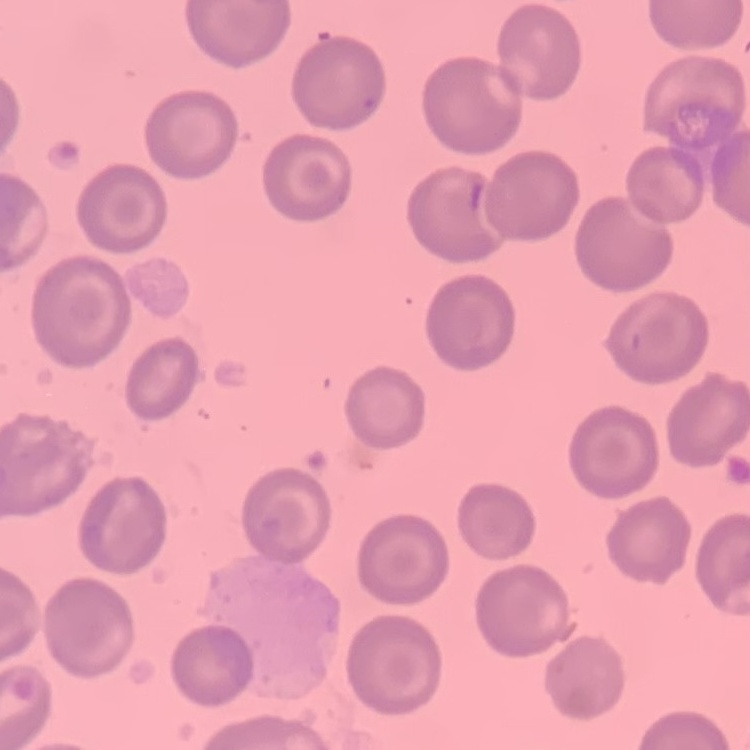
erythrocyte morphology = no rouleaux formation
stain = Field's or Giemsa
image type = one tile cut from a larger photomicrograph
preparation = thin peripheral smear